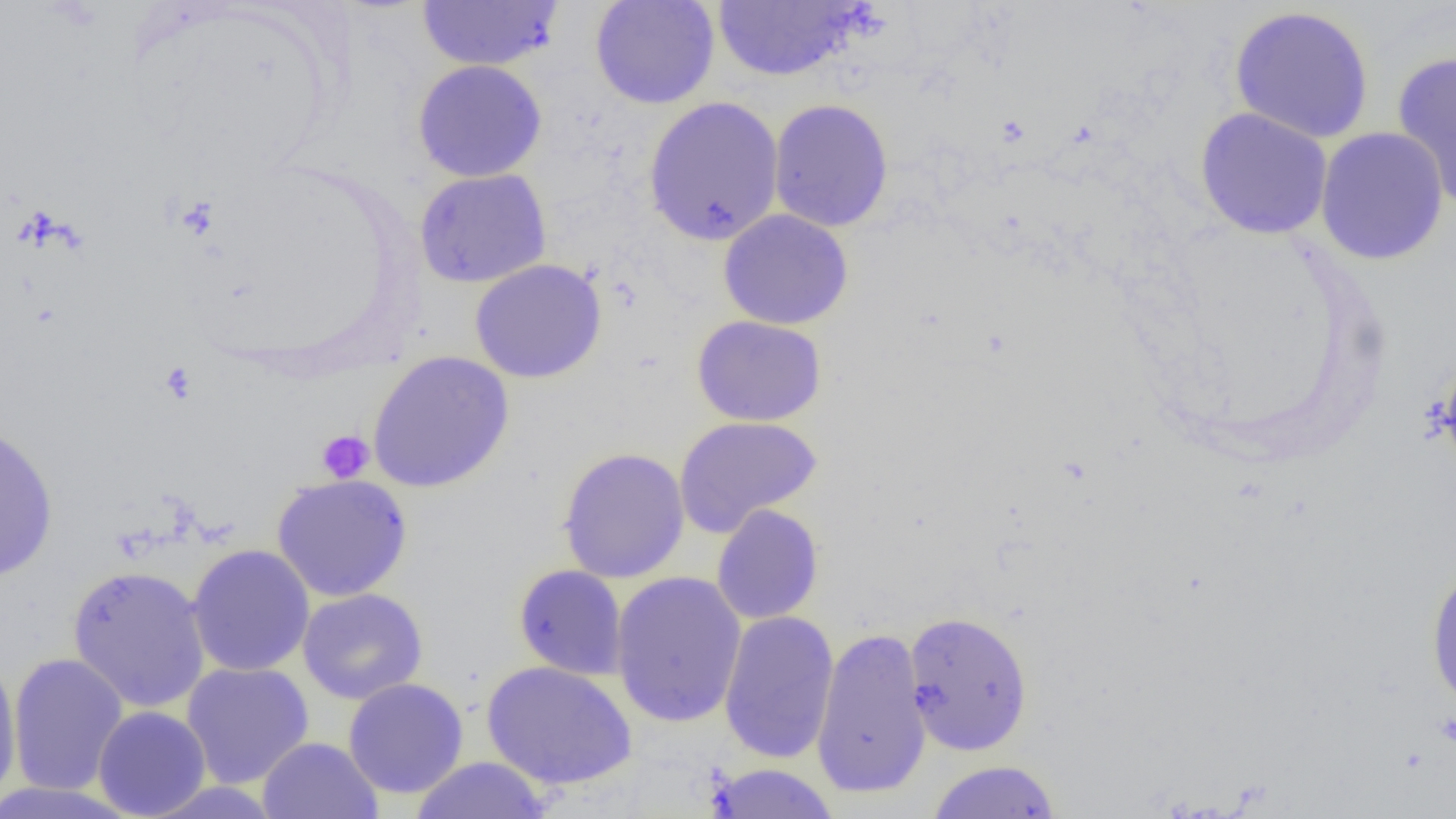 Approximate bounding boxes as [x1, y1, x2, y2] in pixels. Platelet locations: [158, 361, 199, 405], [316, 429, 375, 484]. Uninfected red blood cell locations: [416, 0, 564, 71], [590, 0, 720, 110], [711, 1, 865, 82], [1228, 5, 1375, 144], [1391, 50, 1456, 210], [412, 59, 547, 182], [643, 96, 784, 246], [768, 98, 894, 232], [1194, 107, 1333, 240], [1315, 126, 1449, 266], [414, 168, 552, 288], [718, 209, 854, 330], [469, 258, 607, 383], [692, 315, 827, 426], [367, 351, 514, 493], [1437, 352, 1456, 479], [673, 415, 823, 537], [0, 423, 59, 583], [557, 447, 690, 583], [271, 474, 413, 601], [711, 504, 824, 625], [187, 544, 315, 677], [1425, 563, 1456, 715], [513, 564, 628, 681], [67, 565, 211, 713], [610, 571, 747, 729], [297, 587, 428, 705], [718, 610, 839, 764], [903, 611, 1033, 756], [811, 627, 932, 799], [8, 652, 128, 795], [0, 653, 22, 807], [482, 660, 637, 791], [181, 661, 315, 788], [343, 677, 469, 799], [92, 706, 212, 818], [257, 736, 383, 819], [409, 756, 553, 818], [925, 759, 1062, 818], [704, 762, 841, 819], [0, 782, 139, 818]. Slide-level diagnosis: negative for blood parasites. Single field of view. Captured at 1000x magnification. Thin blood smear. Light microscopy. Image is 1456×819 pixels.